Report the malaria status of this cell.
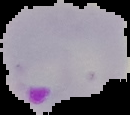

Parasitized.

From a thin blood film. Image is 130×115 pixels. Segmented cell region on a black background.